Classify the preparation.
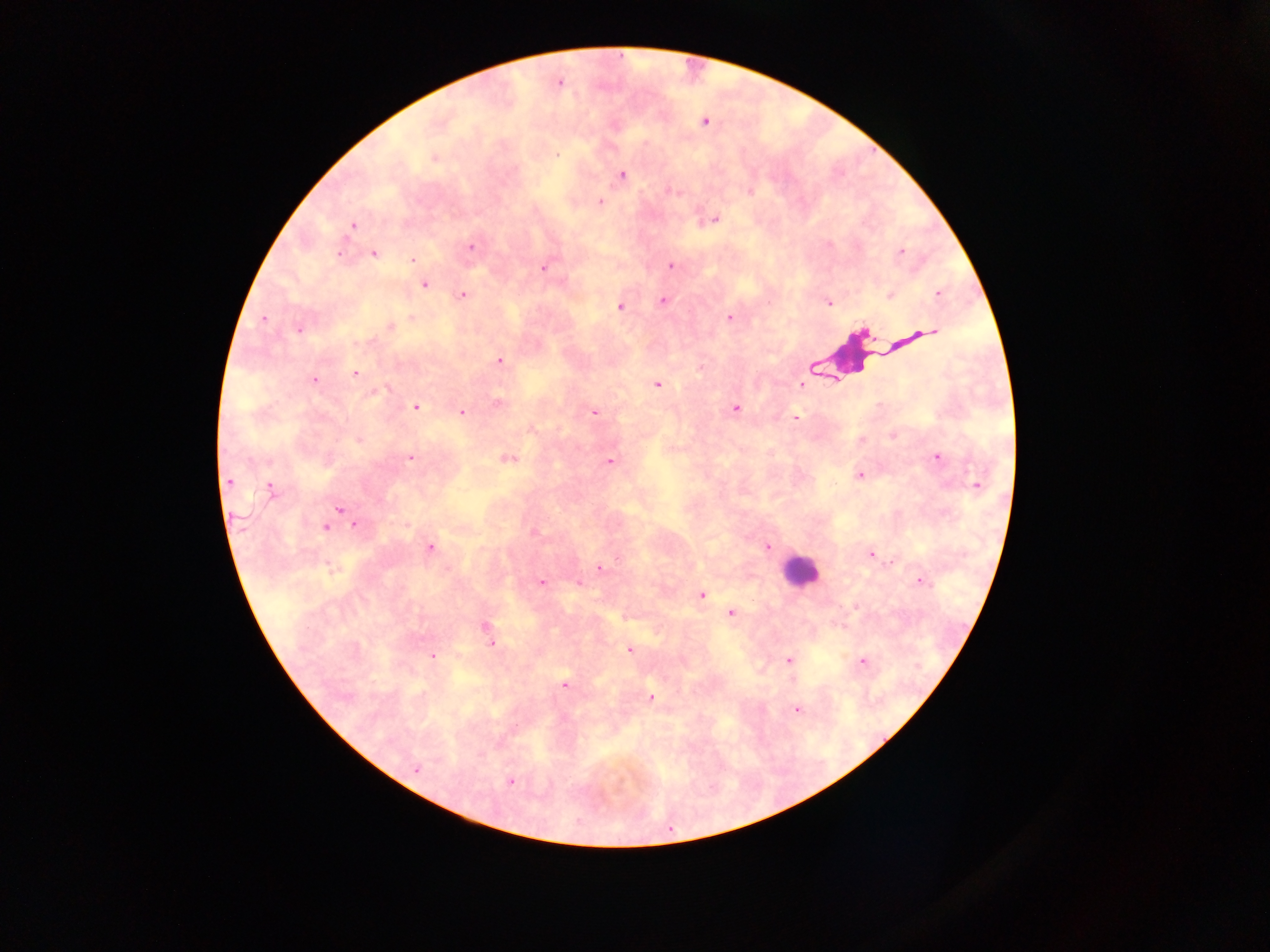
Thick blood film.

Approximate centers as (x, y) in pixels. Plasmodium parasite locations: (559, 85), (704, 121), (558, 153), (434, 157), (621, 175), (672, 190), (750, 190), (599, 201), (716, 218), (353, 226), (469, 246), (899, 250), (374, 253), (413, 260), (671, 264), (545, 266), (424, 283), (937, 294), (462, 296), (890, 297), (662, 300), (829, 304), (620, 307), (410, 315), (264, 318), (729, 318), (390, 326), (297, 330), (926, 331), (862, 333), (915, 333), (500, 360), (355, 374), (314, 379), (801, 383), (658, 386), (497, 403), (416, 406), (735, 408), (462, 412), (595, 412), (796, 417), (532, 429), (892, 436), (358, 440), (409, 456), (936, 456), (506, 457), (610, 461), (859, 476), (227, 480), (270, 487), (339, 509), (355, 526), (326, 528), (534, 531), (767, 546), (431, 547), (869, 553), (598, 567), (329, 569), (542, 582), (579, 582), (918, 582), (701, 595), (731, 614), (624, 616), (487, 627), (491, 644), (628, 648), (433, 656), (787, 661), (863, 661), (790, 680), (565, 684), (652, 697), (797, 709), (498, 743), (416, 770), (511, 783). Leukocyte locations: (854, 361), (795, 571). One field of view. Image is 1270×952 pixels. Sample from Ghana. Photographed through a microscope with a mobile-phone camera.